Report the malaria status of this cell.
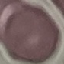

Uninfected.

Summary:
  - Image type: cell patch, automatically extracted from a larger field of view and resized to 64 × 64 pixels
  - Preparation: thin blood film
  - Stain: Giemsa
  - Capture: smartphone camera at the microscope eyepiece